Report the malaria status of this cell.
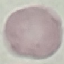

It is uninfected.

Summary:
  - Capture: smartphone camera at the microscope eyepiece
  - Stain: Giemsa
  - Preparation: thin blood smear
  - Image type: cell patch, automatically extracted from a larger field of view and resized to 64 × 64 pixels